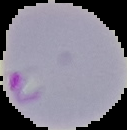

Summary:
  - Result: Plasmodium parasites identified
  - Image size: 127×130 pixels
  - Preparation: thin blood smear
  - Image type: segmented cell region on a black background